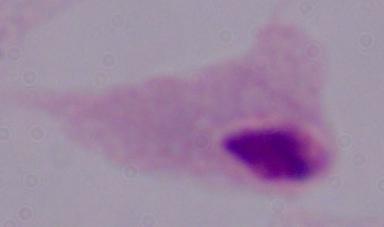 1000x magnification. A trichomonad is seen. Photomicrograph.